Name the parasite shown.
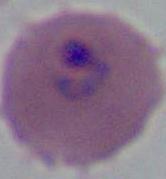

This is Plasmodium.

Micrograph. 400x or 1000x magnification.